Assess this cell for malaria.
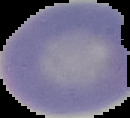
Uninfected.

image_type: segmented cell region on a black background
preparation: thin blood film
image_size: 130×118 pixels